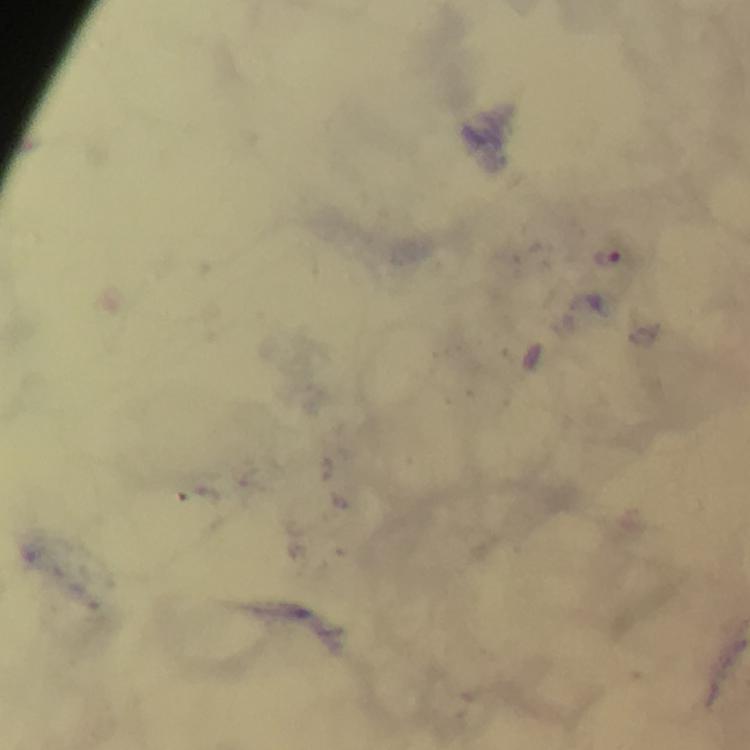

stain = Giemsa
immersion oil = used
magnification = 100x
image size = 750×750 pixels
preparation = thick smear
capture = smartphone mounted on the microscope
cropped from = a single field of view
context = from a malaria diagnostic workup
malaria parasite locations = approximate object centers, in pixels from the top-left corner: (x=606, y=257)